Assess this cell for malaria.
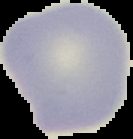

It is uninfected.

Segmented cell region on a black background. Image is 133×139 pixels. From a thin blood film.